State the preparation type.
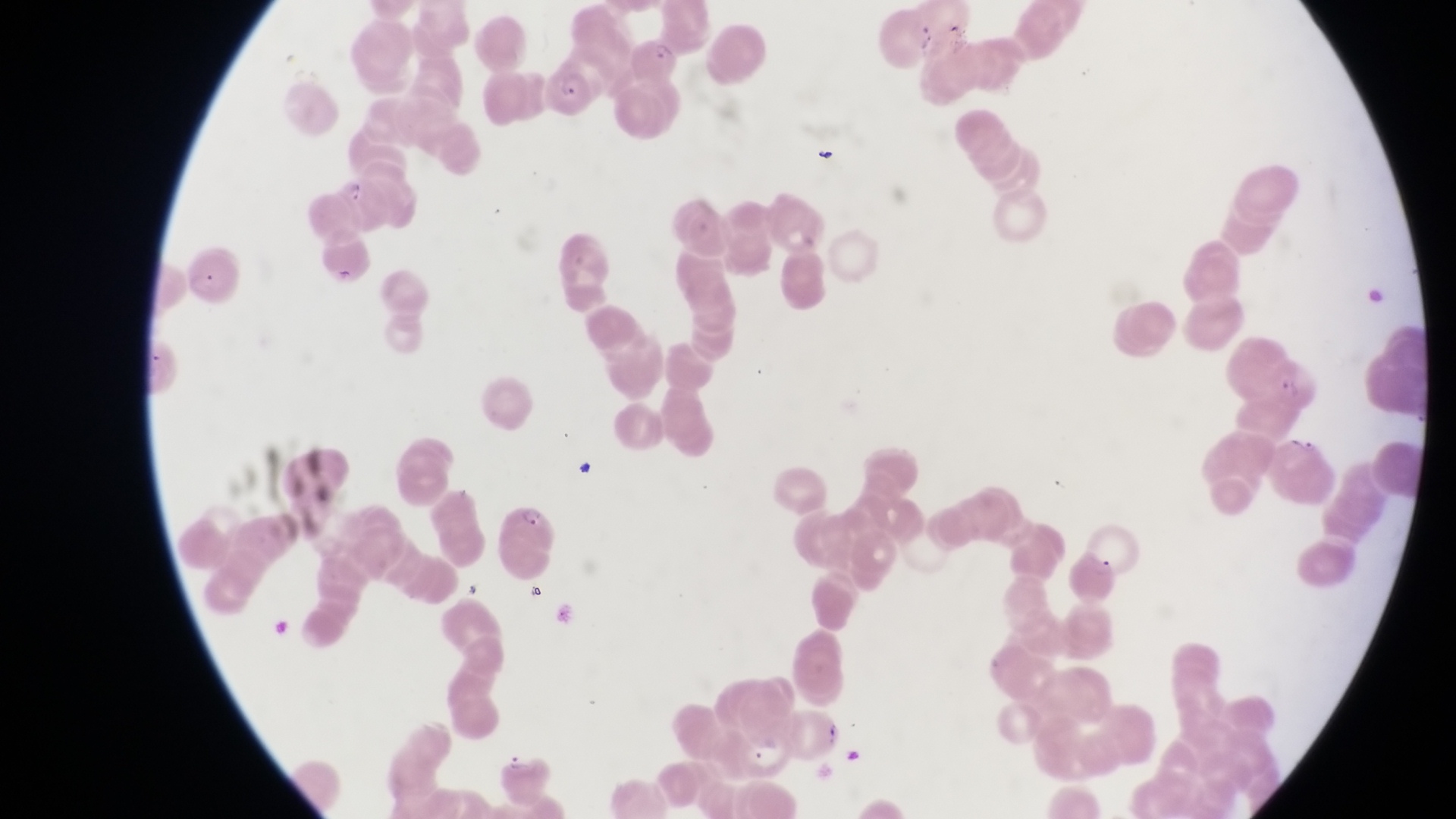
Thin blood smear.

trophozoite locations = approximate bounding boxes as left top right bottom in pixels: 336 175 368 205
magnification = 1000x
capture = smartphone photograph through the eyepiece of an Olympus CX-23 microscope
field of view = single
artifact (platelet-like body, stain precipitate, or debris) locations = approximate bounding boxes as left top right bottom in pixels: 943 23 972 57; 812 146 841 172; 576 457 609 490
parasitised red blood cell locations = approximate bounding boxes as left top right bottom in pixels: 634 32 684 91; 544 60 599 120; 188 240 243 304; 1266 351 1319 410; 505 497 557 583; 1081 516 1140 580
country = Uganda
image size = 1456×819 pixels